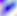

Summary:
  - Identification: Toxoplasma gondii
  - Magnification: 400x
  - Modality: photomicrograph